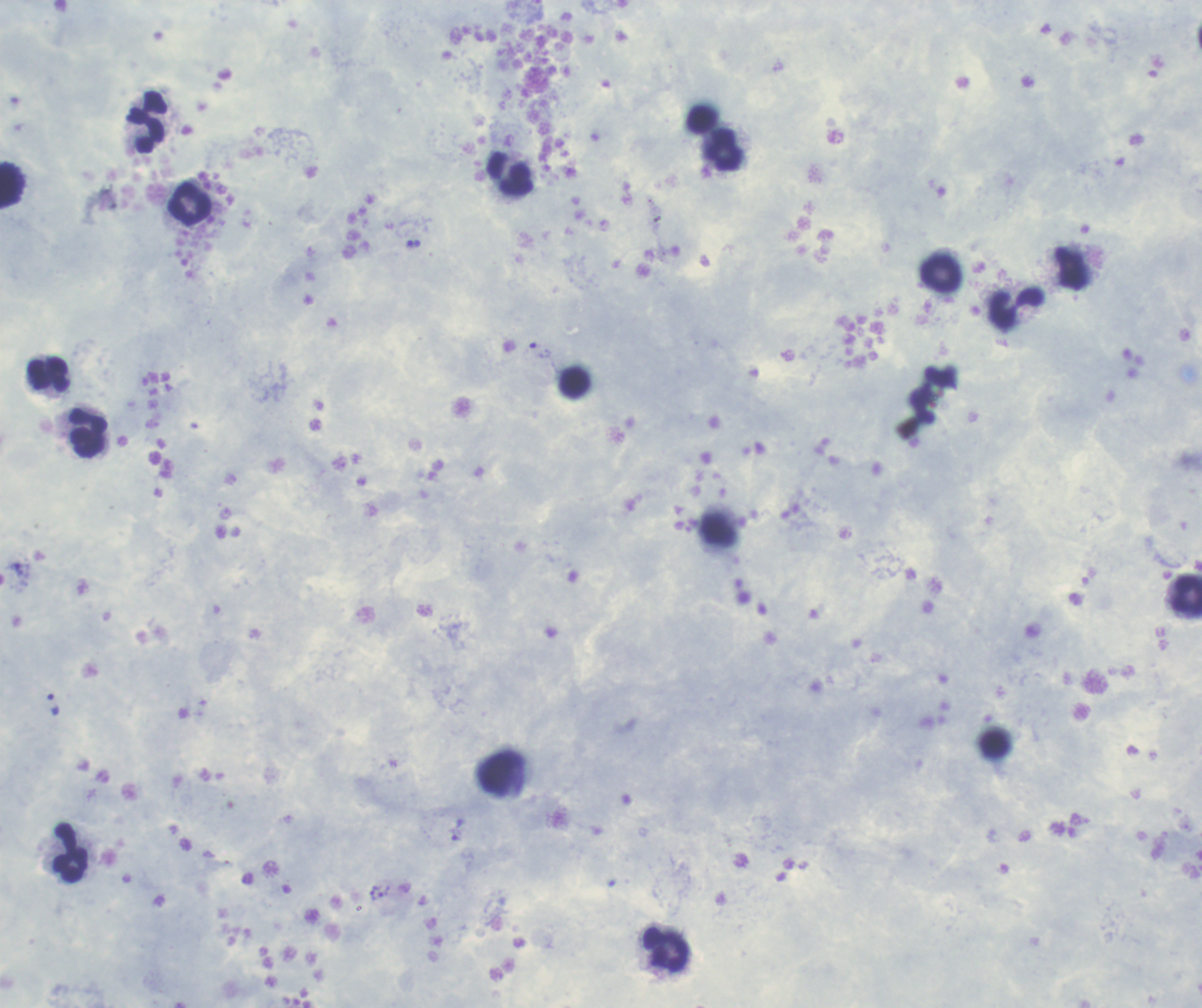
Coloration quality: good. Single field of view. Thick blood smear. Image is 1202×1008 pixels. Romanowsky stain.